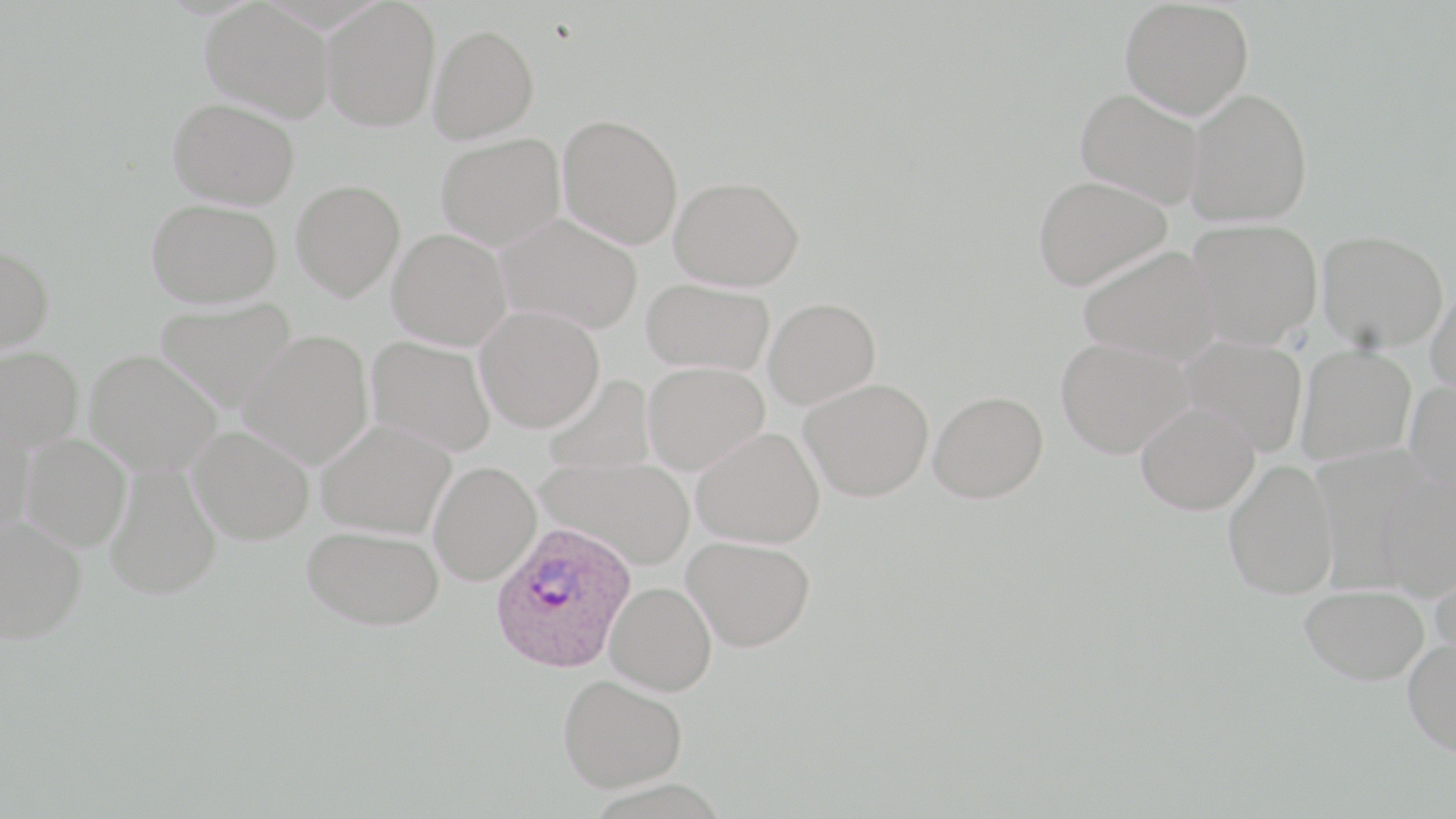 Approximate bounding boxes as named x1/y1/x2/y2 corners in pixels. Uninfected red blood cell locations: (x1=1119, y1=0, x2=1254, y2=118), (x1=201, y1=1, x2=335, y2=122), (x1=320, y1=1, x2=441, y2=131), (x1=428, y1=24, x2=540, y2=143), (x1=1075, y1=87, x2=1207, y2=209), (x1=1185, y1=88, x2=1313, y2=226), (x1=168, y1=98, x2=300, y2=208), (x1=557, y1=114, x2=683, y2=249), (x1=436, y1=133, x2=566, y2=249), (x1=1032, y1=174, x2=1172, y2=291), (x1=669, y1=176, x2=804, y2=291), (x1=291, y1=179, x2=405, y2=301), (x1=146, y1=198, x2=282, y2=307), (x1=495, y1=213, x2=643, y2=335), (x1=1186, y1=217, x2=1322, y2=348), (x1=388, y1=228, x2=512, y2=350), (x1=1317, y1=229, x2=1449, y2=352), (x1=0, y1=243, x2=54, y2=355), (x1=1077, y1=245, x2=1225, y2=365), (x1=641, y1=278, x2=775, y2=376), (x1=1426, y1=283, x2=1456, y2=407), (x1=763, y1=297, x2=881, y2=409), (x1=155, y1=298, x2=298, y2=409), (x1=475, y1=305, x2=605, y2=433), (x1=238, y1=329, x2=374, y2=469), (x1=366, y1=335, x2=496, y2=458), (x1=1177, y1=336, x2=1308, y2=456), (x1=1056, y1=337, x2=1192, y2=458), (x1=1295, y1=345, x2=1416, y2=465), (x1=1, y1=346, x2=84, y2=453), (x1=84, y1=349, x2=223, y2=476), (x1=642, y1=361, x2=769, y2=475), (x1=542, y1=374, x2=657, y2=477), (x1=801, y1=378, x2=934, y2=501), (x1=1405, y1=381, x2=1456, y2=501), (x1=928, y1=391, x2=1048, y2=503), (x1=1135, y1=400, x2=1260, y2=514), (x1=316, y1=418, x2=455, y2=538), (x1=0, y1=419, x2=35, y2=538), (x1=188, y1=425, x2=315, y2=545), (x1=692, y1=427, x2=825, y2=549), (x1=20, y1=433, x2=131, y2=552), (x1=535, y1=456, x2=694, y2=569), (x1=1222, y1=459, x2=1339, y2=599), (x1=104, y1=461, x2=222, y2=600), (x1=428, y1=462, x2=541, y2=585), (x1=1376, y1=476, x2=1456, y2=601), (x1=0, y1=515, x2=86, y2=643), (x1=302, y1=525, x2=444, y2=631), (x1=681, y1=535, x2=814, y2=651), (x1=1430, y1=554, x2=1456, y2=667), (x1=604, y1=581, x2=717, y2=696), (x1=1300, y1=583, x2=1429, y2=684), (x1=1402, y1=637, x2=1456, y2=756), (x1=558, y1=673, x2=687, y2=792). Plasmodium ovale-infected red blood cell locations: (x1=490, y1=519, x2=636, y2=675). Slide-level diagnosis: Plasmodium ovale. Optical microscopy. Single field of view. May-Grünwald-Giemsa stain. Captured at 1000x magnification. Thin blood film. Image is 1456×819 pixels.